Describe the morphology of the red blood cells.
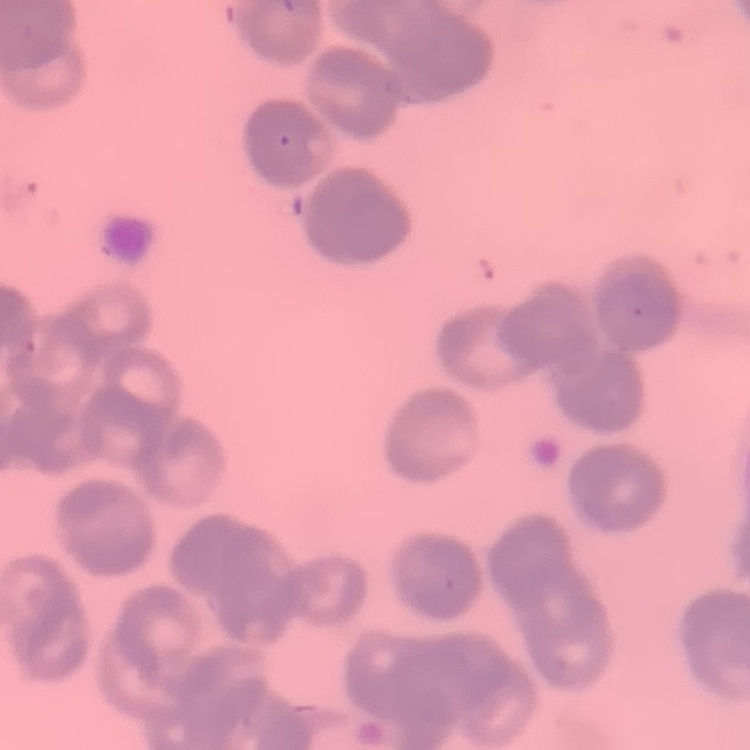
Rouleaux formation.

image type = one tile cut from a larger photomicrograph
stain = Field's or Giemsa
preparation = thin blood smear